Evaluate for Plasmodium parasites.
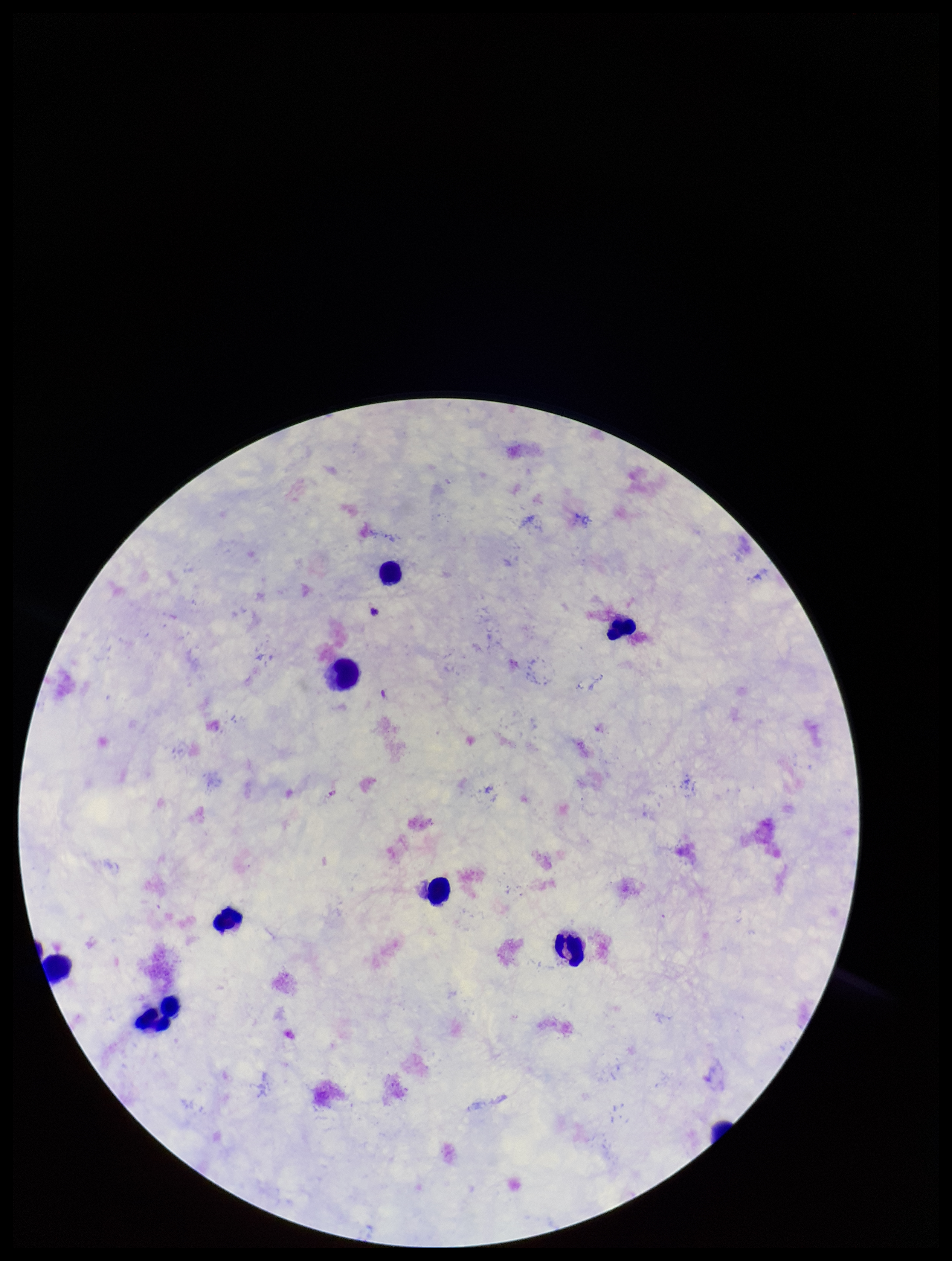

None detected.

Summary:
  - Preparation: thick blood smear
  - Capture: smartphone photograph through the microscope eyepiece
  - Stain: Giemsa
  - Patient malaria status: negative
  - Leukocyte count: 9
  - Image size: 952×1261 pixels
  - Parasite count: 0
  - Field of view: single